Report the malaria status of this cell.
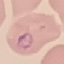

It is parasitized.

{
  "capture": "smartphone through the microscope eyepiece",
  "image_type": "cell patch, automatically extracted from a larger field of view and resized to 64 × 64 pixels",
  "preparation": "thin blood film",
  "stain": "Giemsa"
}